Report the malaria status of this cell.
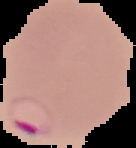
It is parasitized.

Summary:
  - Image size: 136×148 pixels
  - Preparation: thin blood film
  - Image type: cell region segmented out of the field of view; surrounding area masked to black